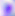
Summary:
  - Magnification: 400x
  - Identification: Toxoplasma gondii
  - Modality: photomicrograph